Comment on the morphology of the red blood cells.
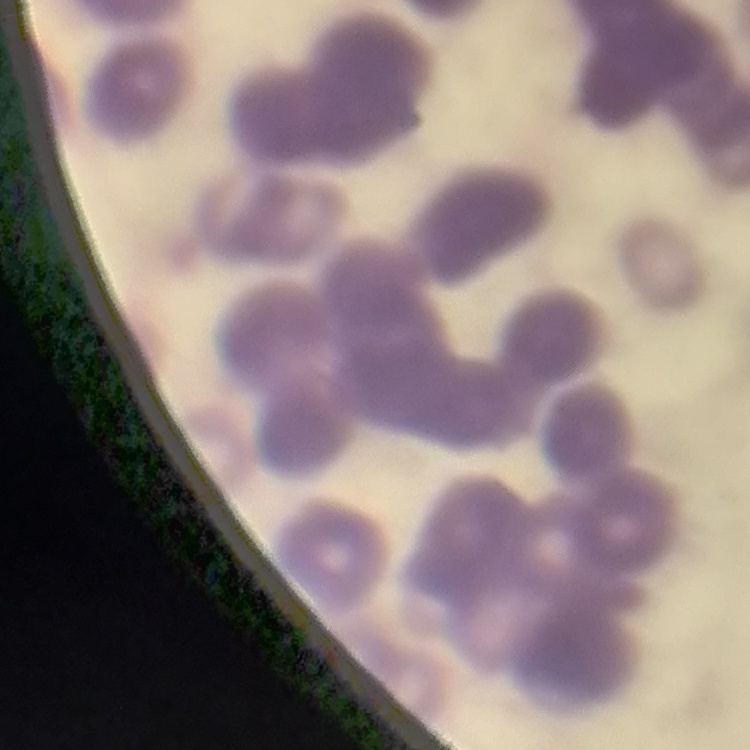

They show rouleaux formation.

Field's or Giemsa stain. Thin blood smear. Square crop of a larger photomicrograph.